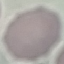

Result: no malaria parasites detected. Thin smear of blood. Acquired by smartphone through the microscope eyepiece. Automatically extracted cell patch, resized to 64 × 64 pixels. Giemsa-stained preparation.